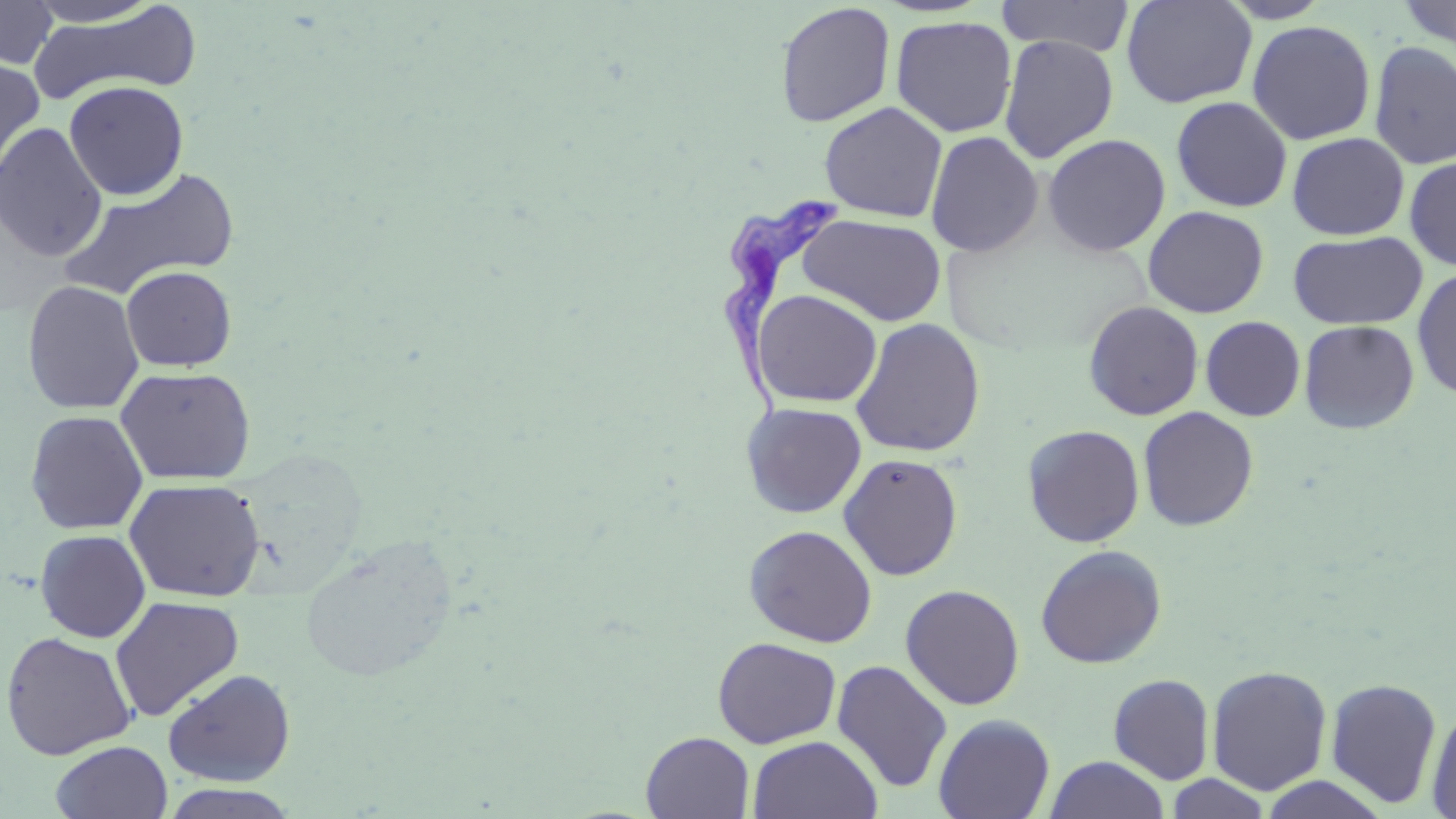
Summary:
  - Coordinate format: approximate bounding boxes as (x1,y1)-(x2,y2) corner pairs in pixels
  - Uninfected red blood cell locations: (23,0)-(165,27), (997,0)-(1136,58), (1120,0)-(1257,108), (1216,0)-(1335,23), (1399,0)-(1455,52), (0,1)-(58,69), (775,2)-(896,128), (27,4)-(202,104), (890,15)-(1017,138), (1246,20)-(1377,145), (998,34)-(1119,163), (1369,41)-(1456,170), (0,56)-(45,182), (64,80)-(188,200), (1171,96)-(1293,213), (820,102)-(948,222), (0,122)-(108,262), (925,131)-(1044,257), (1287,132)-(1409,240), (1042,133)-(1170,256), (1404,155)-(1456,271), (58,167)-(240,299), (1142,205)-(1269,318), (797,213)-(947,326), (1288,231)-(1428,330), (121,265)-(237,371), (1411,267)-(1456,400), (22,280)-(144,415), (752,289)-(883,408), (1084,300)-(1204,420), (1200,316)-(1306,421), (850,318)-(986,458), (1298,320)-(1420,434), (115,366)-(256,485), (741,402)-(866,518), (1138,406)-(1259,531), (25,410)-(148,535), (1022,425)-(1145,548), (235,449)-(367,585), (838,453)-(964,581), (124,478)-(265,602), (743,524)-(878,647), (35,529)-(151,642), (297,535)-(459,683), (1035,544)-(1167,669), (900,584)-(1025,711), (109,595)-(245,722), (1,631)-(136,760), (713,636)-(842,748), (831,659)-(953,793), (1206,665)-(1332,796), (163,668)-(296,786), (1108,673)-(1215,784), (1325,678)-(1443,808), (1426,702)-(1456,818), (933,714)-(1055,819), (640,732)-(755,818), (748,735)-(883,819), (50,740)-(173,819), (1044,755)-(1170,819), (1164,773)-(1273,818), (1257,774)-(1389,818), (159,783)-(301,819)
  - Trypanosoma brucei locations: (719,197)-(838,433)
  - Slide-level diagnosis: Trypanosoma brucei
  - Modality: light microscopy
  - Magnification: 1000x
  - Preparation: thin blood smear
  - Stain: May-Grünwald-Giemsa
  - Image size: 1456×819 pixels
  - Field of view: one of a larger specimen